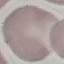

result = no malaria parasites seen
preparation = thin blood smear
capture = smartphone through the microscope eyepiece
stain = Giemsa
image type = automatically extracted cell patch, resized to 64 × 64 pixels